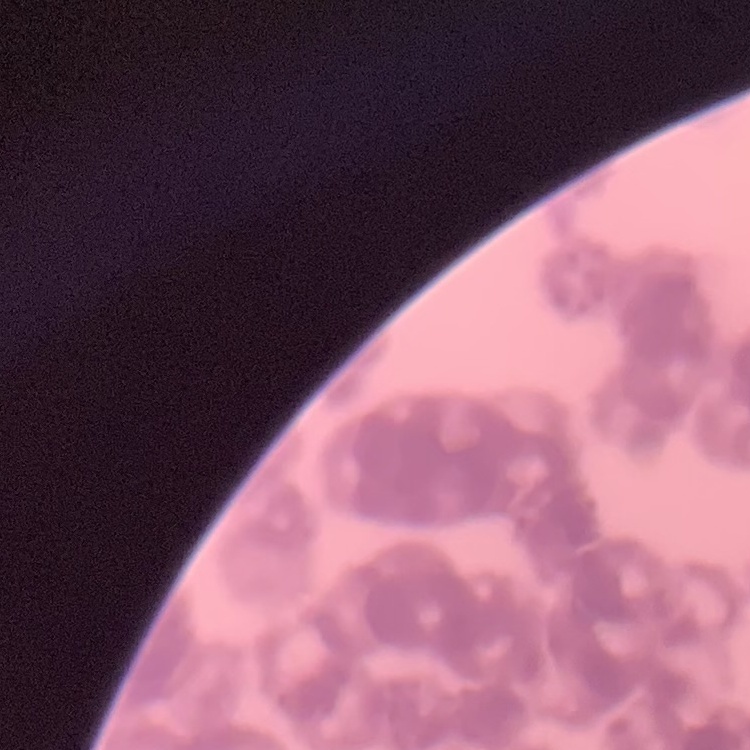
The red blood cells show rouleaux formation. Field's or Giemsa stain. One tile cut from a larger photomicrograph. Thin blood film.